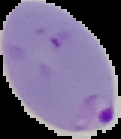
{
  "image_type": "segmented cell region with the area outside set to black",
  "preparation": "thin blood film",
  "malaria_status": "parasitized",
  "image_size": "121×139 pixels"
}